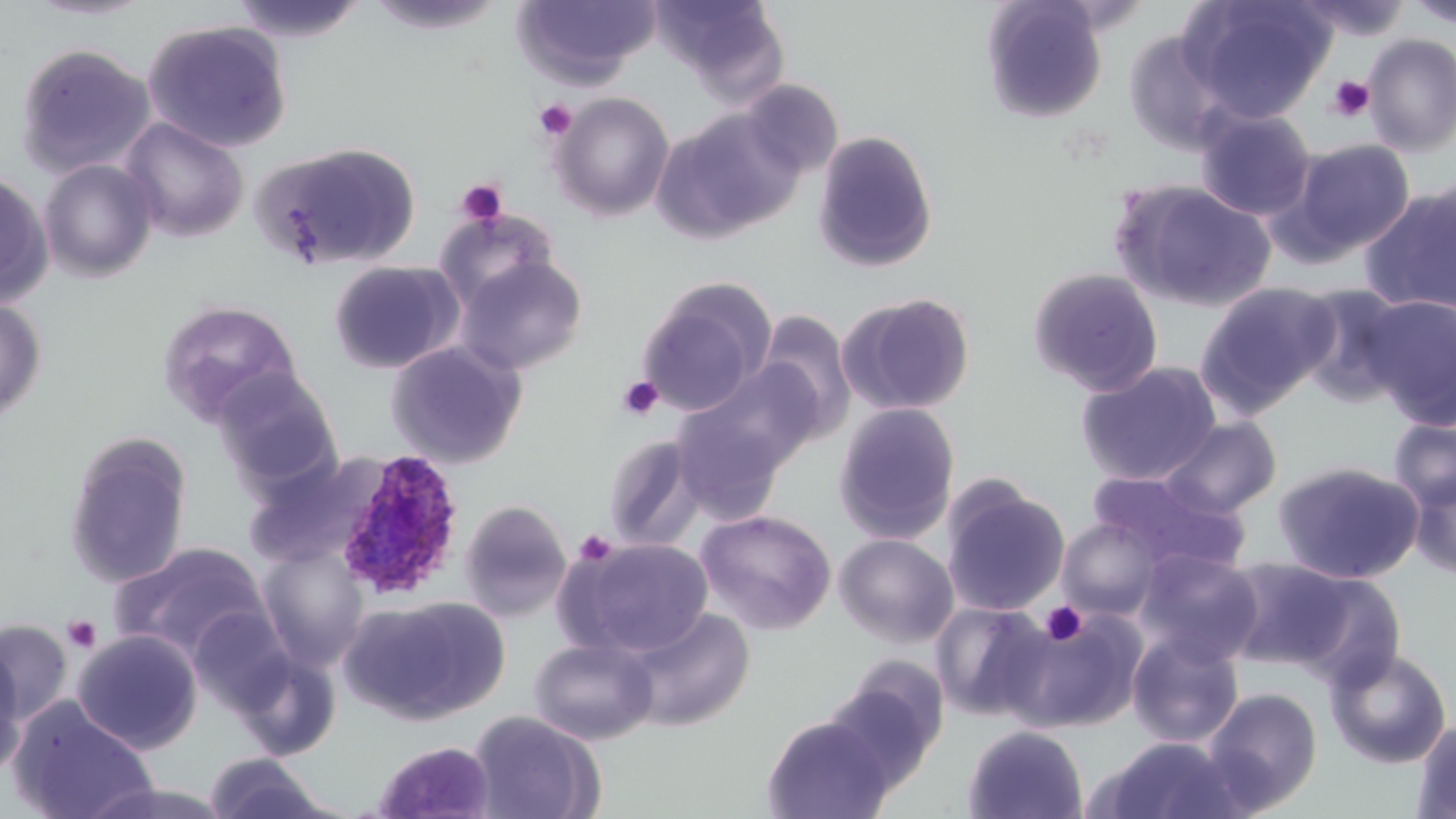
Summary:
  - Coordinate format: approximate bounding boxes as (x1, y1, x2, y2) in pixels
  - Platelet locations: (1326, 75, 1375, 122), (534, 99, 578, 142), (455, 178, 508, 227), (617, 375, 663, 420), (574, 530, 616, 567), (1041, 602, 1087, 645), (62, 615, 103, 654)
  - Plasmodium ovale-infected red blood cell locations: (330, 449, 466, 601)
  - Uninfected red blood cell locations: (25, 0, 156, 22), (228, 0, 370, 43), (364, 0, 509, 34), (511, 0, 660, 87), (651, 0, 788, 94), (980, 0, 1109, 123), (1179, 0, 1336, 123), (1289, 0, 1413, 41), (1406, 1, 1456, 29), (143, 19, 293, 153), (1123, 27, 1236, 156), (1362, 34, 1456, 156), (15, 42, 156, 179), (739, 79, 843, 179), (551, 92, 675, 222), (1195, 107, 1316, 220), (654, 108, 803, 242), (120, 117, 249, 243), (812, 130, 939, 273), (1284, 138, 1416, 261), (254, 141, 421, 271), (39, 158, 159, 283), (0, 171, 54, 307), (1109, 180, 1277, 313), (1360, 185, 1456, 316), (435, 207, 559, 313), (454, 255, 589, 375), (328, 259, 464, 374), (1027, 267, 1164, 396), (635, 278, 775, 417), (1196, 281, 1339, 416), (1296, 284, 1414, 406), (838, 292, 976, 416), (1362, 295, 1456, 429), (0, 297, 47, 425), (156, 299, 304, 428), (755, 310, 857, 440), (385, 340, 528, 470), (674, 360, 821, 491), (1077, 361, 1223, 485), (213, 369, 342, 488), (833, 402, 960, 544), (1160, 415, 1282, 517), (1387, 417, 1456, 513), (63, 432, 193, 589), (603, 432, 709, 552), (242, 453, 387, 571), (1274, 461, 1425, 584), (1407, 468, 1456, 581), (1089, 470, 1249, 576), (941, 479, 1070, 617), (459, 500, 571, 621), (695, 509, 836, 635), (1056, 518, 1162, 620), (834, 533, 959, 648), (562, 537, 714, 658), (109, 542, 272, 663), (256, 545, 371, 670), (1135, 549, 1264, 667), (1220, 557, 1362, 672), (341, 596, 509, 726), (931, 601, 1053, 722), (1005, 606, 1148, 732), (621, 607, 756, 732), (0, 620, 71, 739), (72, 629, 203, 754), (1127, 632, 1244, 748), (529, 637, 659, 746), (0, 639, 28, 780), (225, 646, 342, 761), (1325, 646, 1452, 769), (825, 658, 949, 790), (1201, 686, 1323, 814), (7, 697, 159, 819), (467, 710, 605, 819), (762, 715, 895, 818), (1412, 717, 1456, 818), (963, 725, 1088, 819), (1091, 735, 1247, 819), (373, 741, 497, 818), (203, 752, 334, 818)
  - Slide-level diagnosis: Plasmodium ovale
  - Preparation: thin blood smear
  - Modality: optical microscopy
  - Stain: May-Grünwald-Giemsa
  - Magnification: 1000x
  - Field of view: single
  - Image size: 1456×819 pixels